State which parasite is depicted.
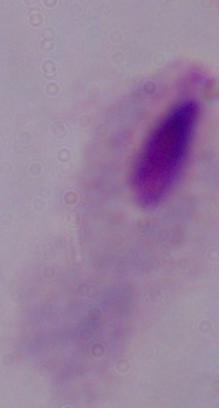
This is a trichomonad.

Captured at 1000x magnification. Photomicrograph.